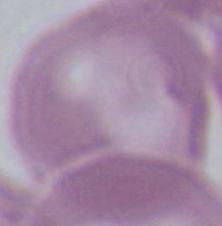
Micrograph. 1000x magnification. An erythrocyte is shown.